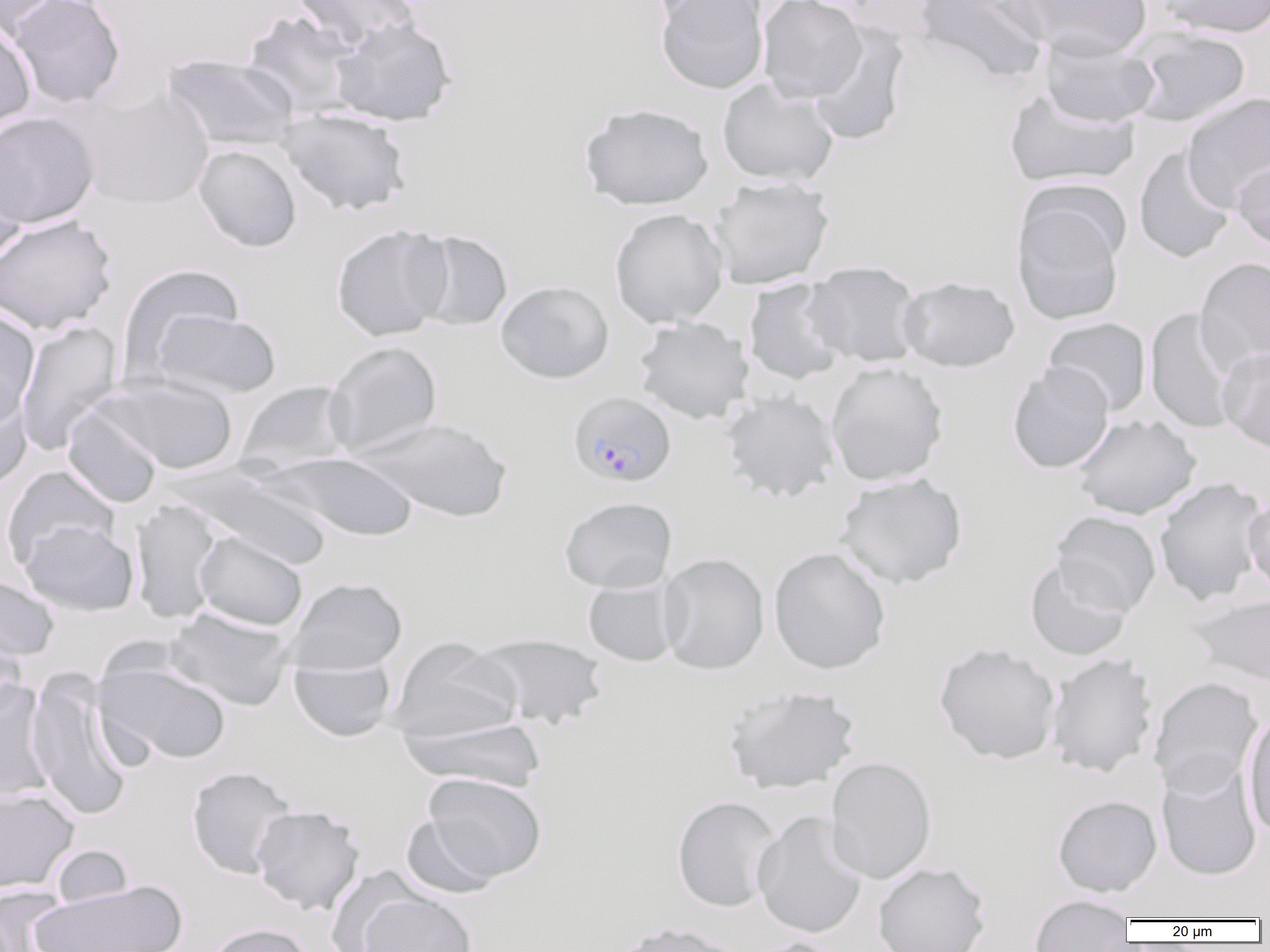 Approximate bounding boxes as named x1/y1/x2/y2 corners in pixels. Plasmodium falciparum-infected red blood cell locations: (x1=568, y1=391, x2=677, y2=488). Uninfected red blood cell locations: (x1=0, y1=0, x2=64, y2=38), (x1=6, y1=0, x2=126, y2=110), (x1=291, y1=0, x2=419, y2=55), (x1=645, y1=0, x2=767, y2=26), (x1=655, y1=0, x2=769, y2=95), (x1=757, y1=0, x2=867, y2=103), (x1=913, y1=0, x2=1051, y2=85), (x1=1011, y1=0, x2=1152, y2=59), (x1=1158, y1=0, x2=1270, y2=38), (x1=242, y1=11, x2=361, y2=118), (x1=330, y1=16, x2=457, y2=127), (x1=0, y1=21, x2=36, y2=134), (x1=808, y1=24, x2=909, y2=147), (x1=1125, y1=27, x2=1251, y2=128), (x1=1039, y1=36, x2=1160, y2=128), (x1=161, y1=53, x2=300, y2=153), (x1=716, y1=78, x2=839, y2=187), (x1=1004, y1=88, x2=1140, y2=189), (x1=73, y1=89, x2=214, y2=209), (x1=1182, y1=91, x2=1270, y2=212), (x1=578, y1=102, x2=714, y2=211), (x1=276, y1=107, x2=412, y2=217), (x1=0, y1=111, x2=100, y2=228), (x1=0, y1=142, x2=30, y2=267), (x1=193, y1=145, x2=301, y2=252), (x1=1133, y1=146, x2=1236, y2=264), (x1=1232, y1=157, x2=1270, y2=251), (x1=708, y1=176, x2=834, y2=290), (x1=1011, y1=191, x2=1127, y2=326), (x1=609, y1=208, x2=728, y2=328), (x1=0, y1=215, x2=118, y2=334), (x1=330, y1=224, x2=453, y2=342), (x1=409, y1=229, x2=513, y2=332), (x1=1194, y1=256, x2=1270, y2=377), (x1=802, y1=260, x2=925, y2=368), (x1=117, y1=263, x2=244, y2=379), (x1=898, y1=276, x2=1020, y2=372), (x1=743, y1=279, x2=849, y2=386), (x1=495, y1=280, x2=614, y2=384), (x1=1145, y1=307, x2=1240, y2=434), (x1=0, y1=309, x2=40, y2=429), (x1=152, y1=309, x2=282, y2=400), (x1=634, y1=317, x2=754, y2=425), (x1=1042, y1=317, x2=1151, y2=417), (x1=15, y1=320, x2=123, y2=455), (x1=323, y1=341, x2=443, y2=458), (x1=1218, y1=346, x2=1270, y2=453), (x1=825, y1=361, x2=949, y2=486), (x1=1006, y1=362, x2=1114, y2=473), (x1=95, y1=374, x2=239, y2=474), (x1=237, y1=381, x2=353, y2=473), (x1=0, y1=384, x2=32, y2=494), (x1=720, y1=390, x2=840, y2=504), (x1=63, y1=404, x2=163, y2=508), (x1=1071, y1=414, x2=1201, y2=520), (x1=354, y1=417, x2=513, y2=523), (x1=261, y1=451, x2=421, y2=542), (x1=176, y1=464, x2=335, y2=569), (x1=1, y1=467, x2=120, y2=569), (x1=835, y1=473, x2=968, y2=589), (x1=1154, y1=476, x2=1268, y2=606), (x1=1243, y1=494, x2=1270, y2=597), (x1=559, y1=496, x2=677, y2=593), (x1=130, y1=499, x2=223, y2=624), (x1=1050, y1=511, x2=1162, y2=616), (x1=19, y1=519, x2=139, y2=616), (x1=194, y1=531, x2=308, y2=631), (x1=768, y1=546, x2=890, y2=674), (x1=658, y1=553, x2=769, y2=675), (x1=1024, y1=559, x2=1132, y2=661), (x1=0, y1=575, x2=60, y2=662), (x1=285, y1=577, x2=408, y2=675), (x1=582, y1=577, x2=681, y2=667), (x1=1189, y1=594, x2=1270, y2=686), (x1=165, y1=607, x2=294, y2=711), (x1=0, y1=630, x2=28, y2=722), (x1=471, y1=632, x2=609, y2=730), (x1=389, y1=636, x2=522, y2=743), (x1=933, y1=641, x2=1061, y2=765), (x1=1046, y1=653, x2=1158, y2=778), (x1=289, y1=656, x2=397, y2=742), (x1=93, y1=657, x2=231, y2=766), (x1=25, y1=672, x2=134, y2=821), (x1=1148, y1=676, x2=1264, y2=797), (x1=0, y1=682, x2=55, y2=806), (x1=721, y1=684, x2=860, y2=794), (x1=1243, y1=710, x2=1270, y2=839), (x1=398, y1=716, x2=547, y2=792), (x1=825, y1=756, x2=936, y2=884), (x1=1156, y1=759, x2=1263, y2=883), (x1=186, y1=766, x2=298, y2=879), (x1=421, y1=772, x2=547, y2=884), (x1=0, y1=788, x2=79, y2=893), (x1=1052, y1=794, x2=1162, y2=897), (x1=671, y1=795, x2=781, y2=912), (x1=250, y1=805, x2=364, y2=915), (x1=752, y1=811, x2=868, y2=939), (x1=402, y1=814, x2=501, y2=899), (x1=50, y1=844, x2=134, y2=910), (x1=873, y1=862, x2=990, y2=952), (x1=32, y1=878, x2=185, y2=952), (x1=1, y1=886, x2=71, y2=952), (x1=357, y1=890, x2=477, y2=952), (x1=1029, y1=894, x2=1134, y2=951), (x1=609, y1=921, x2=746, y2=952), (x1=202, y1=922, x2=316, y2=952), (x1=743, y1=937, x2=850, y2=952). Slide-level diagnosis: Plasmodium falciparum. Image is 1270×952 pixels. Thin blood smear. Single field of view. Optical microscopy. Captured at 1000x magnification.